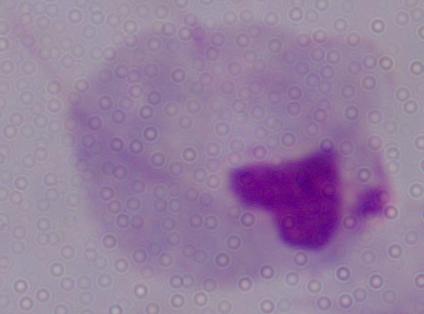

Summary:
  - Identification: trichomonad
  - Modality: micrograph
  - Magnification: 1000x